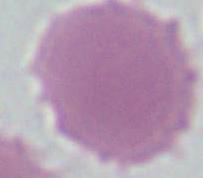
A red blood cell is seen. Photomicrograph. 1000x magnification.